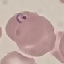

Summary:
  - Malaria status: parasitized
  - Stain: Giemsa
  - Image type: automatically extracted cell patch, resized to 64 × 64 pixels
  - Preparation: thin blood smear
  - Capture: smartphone through the microscope eyepiece